Classify this cell by malaria status.
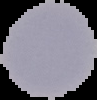

Uninfected.

Summary:
  - Image size: 97×100 pixels
  - Preparation: thin blood film
  - Image type: segmented cell region with the area outside set to black